Identify the parasite.
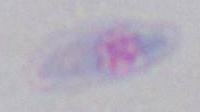
This is Toxoplasma gondii.

Summary:
  - Modality: photomicrograph
  - Magnification: 1000x